Assess this cell for malaria.
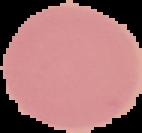

Uninfected.

image size = 142×133 pixels
image type = segmented cell region with the area outside set to black
preparation = thin blood smear